Classify this cell by malaria status.
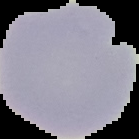
Uninfected.

Summary:
  - Image type: segmented cell region on a black background
  - Image size: 139×139 pixels
  - Preparation: thin blood film